Give the preparation type.
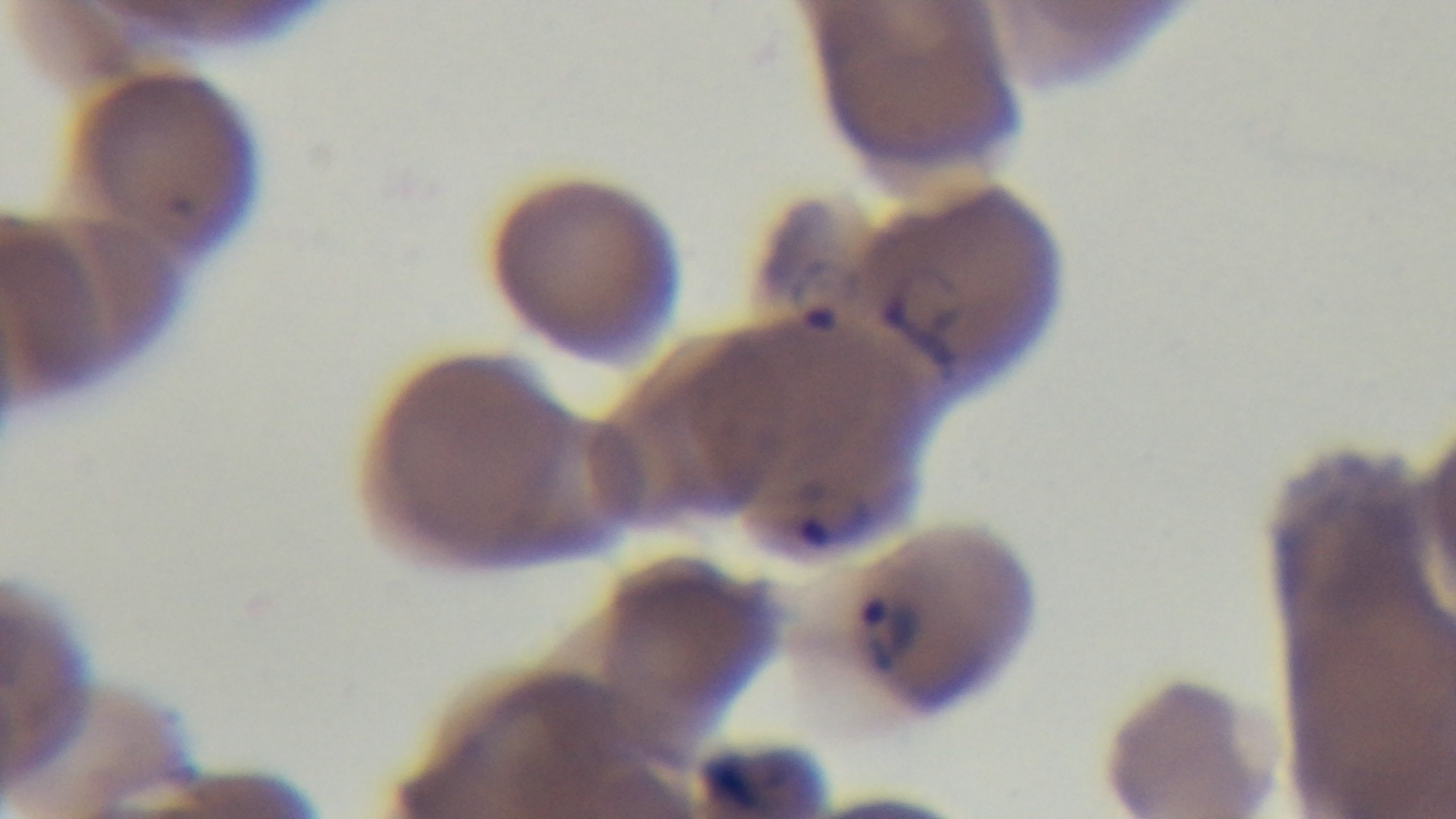
Thin.

Summary:
  - Objective: 100x oil immersion
  - Capture: mounted 4K digital camera
  - Stain: Giemsa
  - Field of view: single
  - Malaria status: positive
  - Modality: light microscopy